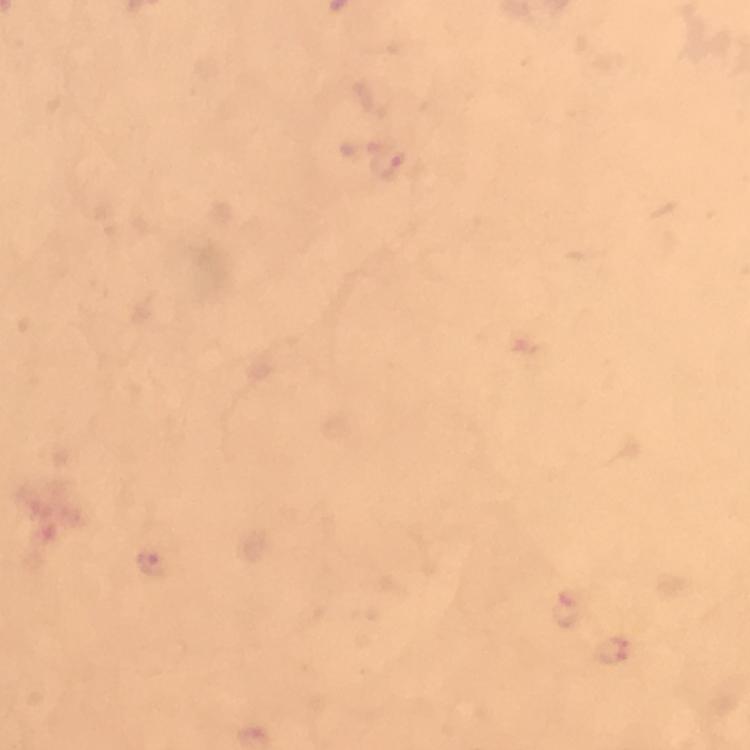

Approximate object centers, in pixels from the top-left corner.
Summary:
  - Malaria parasite locations: (x=388, y=161), (x=151, y=563), (x=564, y=608), (x=609, y=652)
  - Stain: Giemsa
  - Capture: smartphone mounted on the microscope
  - Preparation: thick blood smear
  - Magnification: 100x
  - Immersion oil: used
  - Image size: 750×750 pixels
  - Context: from a malaria diagnostic workup
  - Cropped from: one field of view